Report the malaria status of this cell.
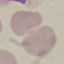

It is uninfected.

image type = automatically extracted cell patch, resized to 64 × 64 pixels
stain = Giemsa
preparation = thin blood smear
capture = smartphone through the microscope eyepiece